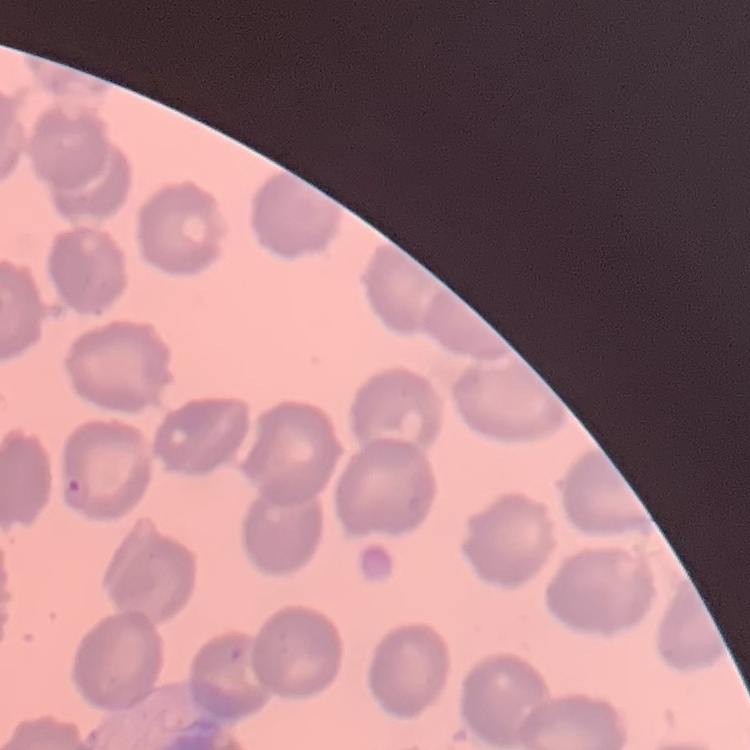

red_blood_cell_morphology: no rouleaux formation
image_type: square crop of a larger photomicrograph
stain: Field's or Giemsa
preparation: thin blood film